Name the cell type shown.
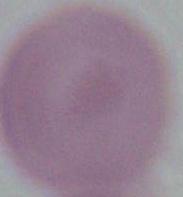

An erythrocyte.

Captured at 1000x magnification. Micrograph.